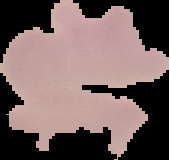
image_type: cell region segmented out of the field of view; surrounding area masked to black
result: negative for malaria parasites
preparation: thin blood smear
image_size: 169×160 pixels